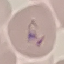 Result: negative for malaria parasites. Photographed with a smartphone camera at the microscope eyepiece. Thin blood film. Cell patch, automatically extracted from a larger field of view and resized to 64 × 64 pixels. Giemsa stain.